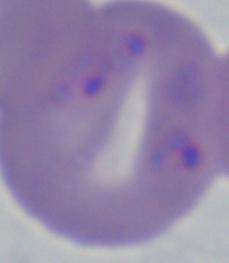
Summary:
  - Magnification: 1000x
  - Modality: micrograph
  - Identification: Babesia